Classify this cell by malaria status.
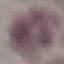

Uninfected.

Summary:
  - Capture: smartphone through the microscope eyepiece
  - Image type: automatically extracted cell patch, resized to 64 × 64 pixels
  - Stain: Giemsa
  - Preparation: thin smear